Name the parasite shown.
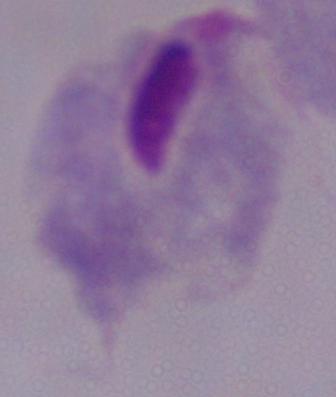
This is a trichomonad.

modality = micrograph
magnification = 1000x